Report the malaria status of this cell.
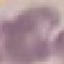

It is uninfected.

stain: Giemsa
preparation: thin blood film
image_type: cell patch, automatically extracted from a larger field of view and resized to 64 × 64 pixels
capture: smartphone camera at the microscope eyepiece